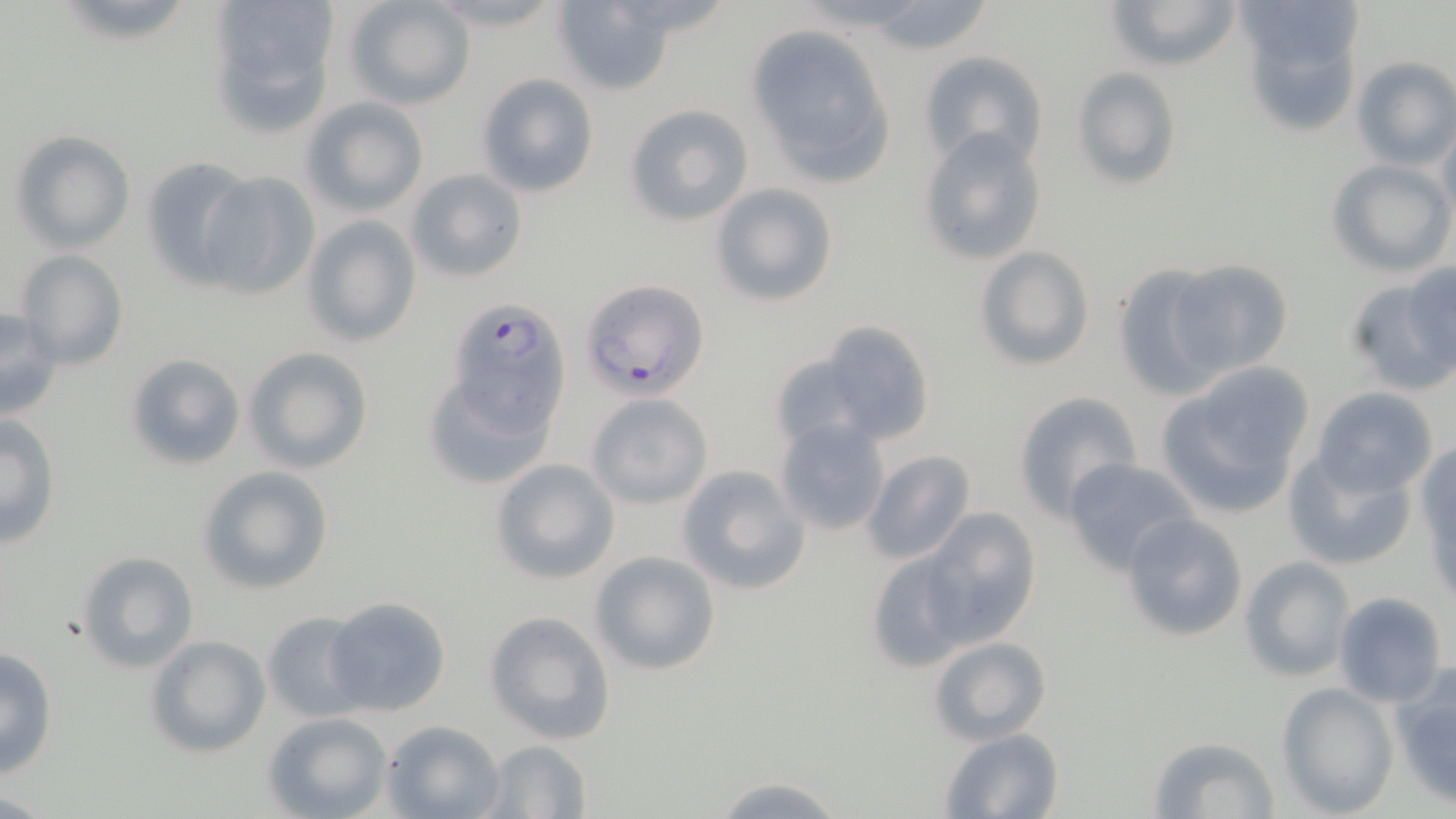

Plasmodium falciparum-infected red blood cell locations = approximate bounding boxes as (x1, y1, x2, y2) in pixels: (581, 278, 711, 399)
slide-level diagnosis = Plasmodium falciparum
field of view = one of a larger specimen
image size = 1456×819 pixels
modality = light microscopy
stain = May-Grünwald-Giemsa
magnification = 1000x
uninfected red blood cell locations = approximate bounding boxes as (x1, y1, x2, y2) in pixels: (208, 0, 341, 135), (1104, 0, 1243, 74), (342, 1, 478, 109), (551, 1, 677, 95), (853, 1, 1005, 57), (1235, 5, 1361, 139), (747, 23, 896, 186), (918, 49, 1048, 171), (1352, 56, 1456, 171), (1070, 67, 1183, 191), (475, 73, 599, 199), (301, 98, 429, 217), (623, 104, 754, 225), (1434, 118, 1456, 229), (9, 130, 135, 253), (918, 130, 1049, 267), (140, 156, 255, 287), (1325, 158, 1454, 276), (405, 167, 530, 283), (195, 170, 321, 301), (711, 184, 838, 305), (299, 215, 423, 349), (975, 246, 1094, 371), (15, 250, 130, 371), (1169, 258, 1293, 381), (1399, 261, 1455, 378), (1111, 262, 1231, 400), (1347, 276, 1452, 398), (448, 296, 568, 452), (0, 306, 66, 422), (817, 319, 936, 447), (243, 346, 375, 473), (768, 349, 877, 451), (125, 354, 247, 471), (422, 359, 557, 487), (1155, 369, 1315, 518), (1310, 386, 1440, 498), (1013, 390, 1142, 517), (586, 392, 714, 510), (0, 413, 62, 548), (773, 416, 892, 536), (1415, 439, 1456, 577), (861, 449, 977, 565), (1284, 449, 1418, 571), (1063, 457, 1199, 575), (489, 458, 621, 584), (678, 464, 811, 596), (197, 466, 334, 594), (916, 509, 1042, 648), (1119, 513, 1249, 641), (866, 546, 978, 669), (588, 550, 721, 677), (77, 551, 200, 674), (1239, 555, 1357, 682), (1334, 592, 1448, 707), (322, 596, 453, 717), (484, 610, 617, 743), (260, 611, 370, 722), (144, 635, 270, 757), (928, 636, 1053, 745), (0, 646, 59, 778), (1389, 662, 1456, 809), (1276, 683, 1399, 816), (262, 711, 394, 819), (380, 720, 506, 819), (940, 728, 1064, 817), (1148, 734, 1280, 816), (481, 739, 593, 818), (710, 772, 848, 818)
preparation = thin blood film